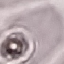

Summary:
  - Malaria status: uninfected
  - Preparation: thin blood film
  - Capture: smartphone camera at the microscope eyepiece
  - Stain: Giemsa
  - Image type: automatically extracted cell patch, resized to 64 × 64 pixels